Name the parasite shown.
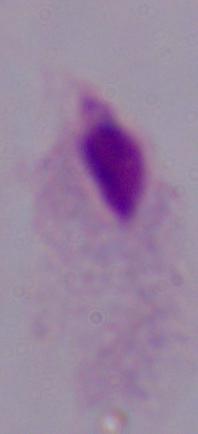

A trichomonad.

Photomicrograph. Captured at 1000x magnification.